Assess this cell for malaria.
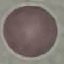
Uninfected.

Summary:
  - Image type: cell patch, automatically extracted from a larger field of view and resized to 64 × 64 pixels
  - Stain: Giemsa
  - Preparation: thin blood film
  - Capture: smartphone camera at the microscope eyepiece